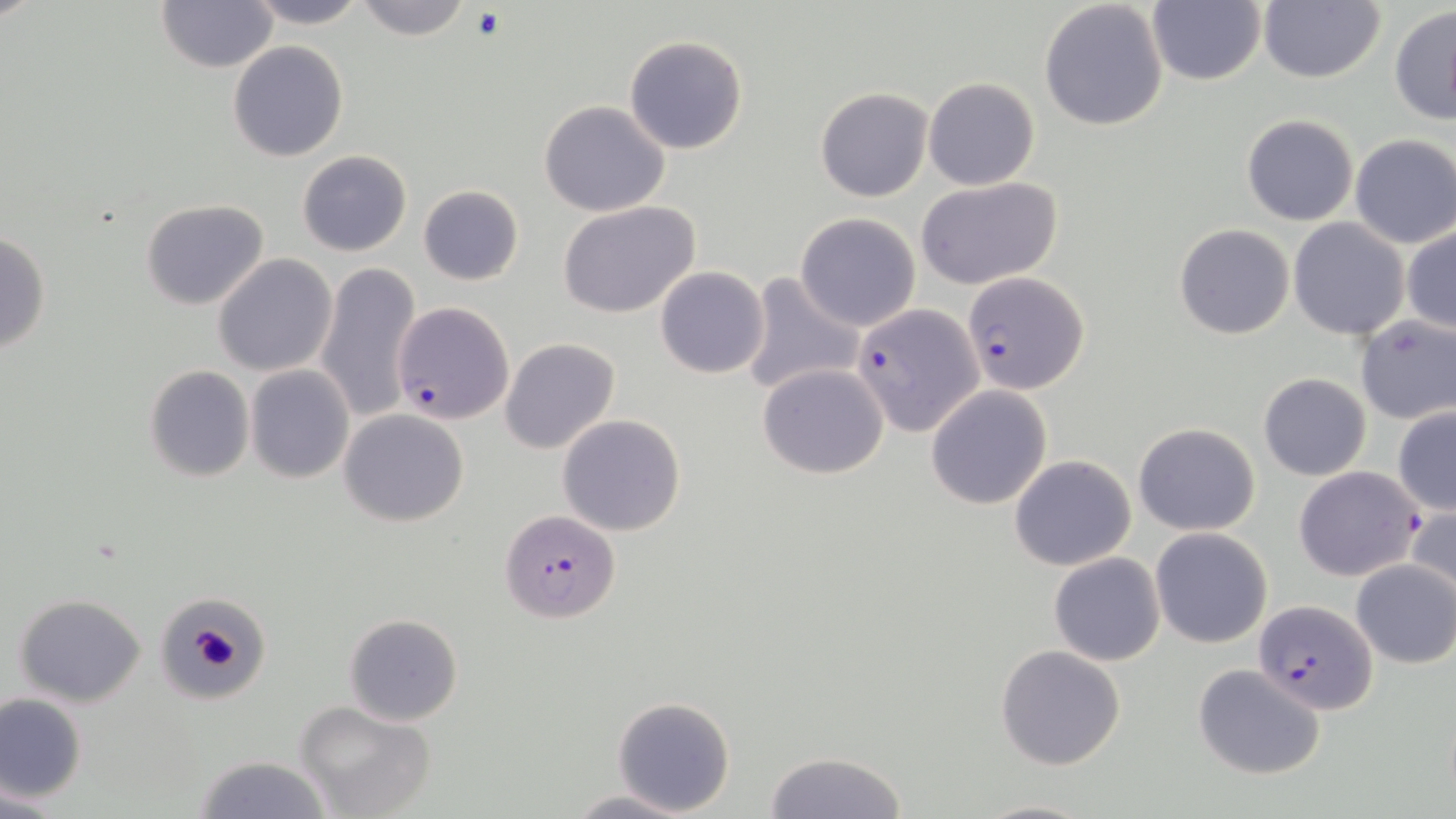
Approximate bounding boxes as (x1,y1)-(x2,y2) corner pairs in pixels. Platelet locations: (192,627)-(240,666). Uninfected red blood cell locations: (241,0)-(369,29), (352,0)-(471,41), (1258,0)-(1385,84), (156,1)-(278,72), (1039,1)-(1170,134), (1146,1)-(1266,86), (1389,5)-(1456,124), (623,34)-(748,155), (227,40)-(348,162), (923,76)-(1039,190), (815,88)-(932,202), (539,100)-(671,217), (1241,114)-(1358,226), (1349,134)-(1456,248), (298,150)-(411,257), (917,176)-(1064,290), (417,184)-(524,286), (141,199)-(269,310), (557,201)-(702,318), (794,213)-(921,331), (1287,217)-(1409,341), (1174,223)-(1295,339), (1402,225)-(1455,335), (0,231)-(51,355), (213,254)-(337,377), (316,261)-(421,424), (655,266)-(770,379), (739,273)-(866,397), (391,301)-(515,425), (1354,315)-(1456,424), (499,338)-(619,455), (757,363)-(889,479), (143,364)-(255,482), (245,365)-(355,483), (1258,373)-(1372,482), (925,385)-(1052,510), (1392,405)-(1456,516), (339,409)-(469,527), (556,414)-(687,537), (1132,422)-(1260,535), (1009,455)-(1136,571), (1405,506)-(1455,610), (1150,528)-(1273,648), (1048,553)-(1165,665), (1351,558)-(1456,668), (155,588)-(272,701), (14,594)-(148,706), (343,613)-(464,726), (995,644)-(1128,771), (1194,663)-(1327,781), (1,693)-(87,802), (614,696)-(734,816), (294,700)-(437,819), (762,750)-(909,819), (191,756)-(336,818), (565,790)-(703,819), (972,796)-(1095,818). Plasmodium falciparum-infected red blood cell locations: (963,270)-(1088,393), (855,303)-(983,436), (1295,466)-(1424,582), (499,510)-(621,624), (1254,599)-(1376,716). Slide-level diagnosis: Plasmodium falciparum. One field of a larger specimen. May-Grünwald-Giemsa-stained preparation. Captured at 1000x magnification. Thin blood smear. Light microscopy. Image is 1456×819 pixels.